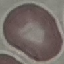
malaria status = uninfected
capture = smartphone through the microscope eyepiece
preparation = thin smear
image type = automatically extracted cell patch, resized to 64 × 64 pixels
stain = Giemsa